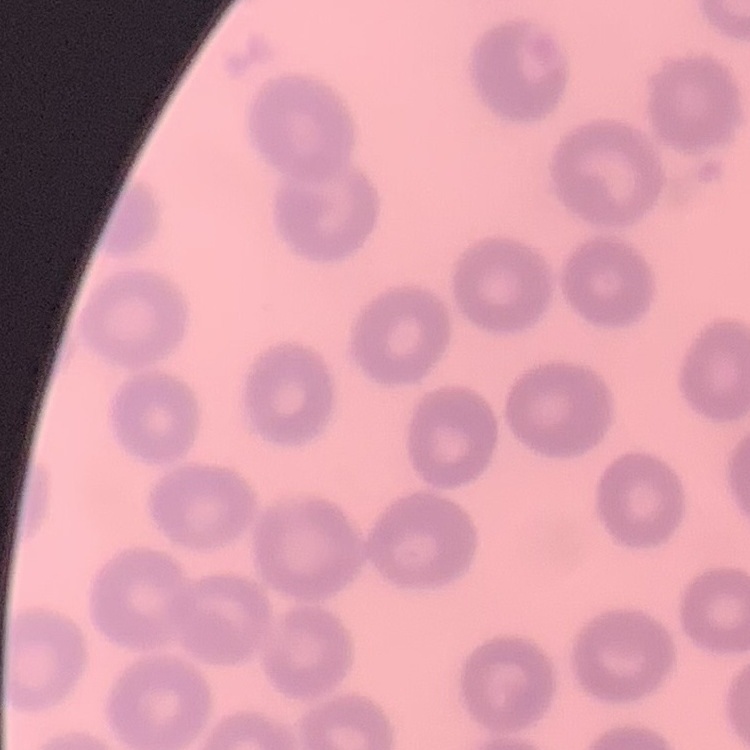
Summary:
  - Red blood cell morphology: no rouleaux formation
  - Stain: Field's or Giemsa
  - Image type: one tile cut from a larger photomicrograph
  - Preparation: thin blood film